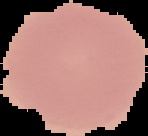

Summary:
  - Image type: segmented cell region with the area outside set to black
  - Preparation: thin blood smear
  - Result: no Plasmodium parasites seen
  - Image size: 148×136 pixels